Assess the morphology of the red blood cells.
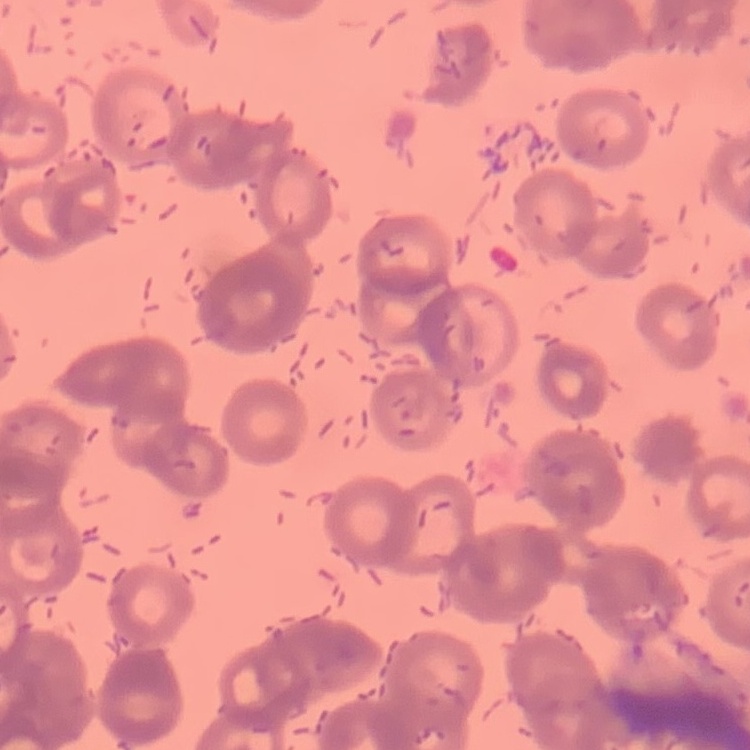

Rouleaux formation.

One tile cut from a larger photomicrograph. Thin blood film. Field's or Giemsa stain.